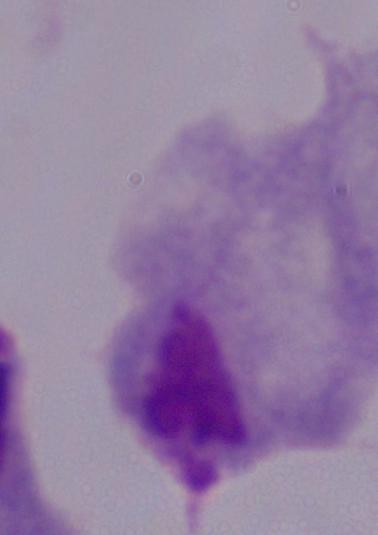

Captured at 1000x magnification. Micrograph. A trichomonad is shown.